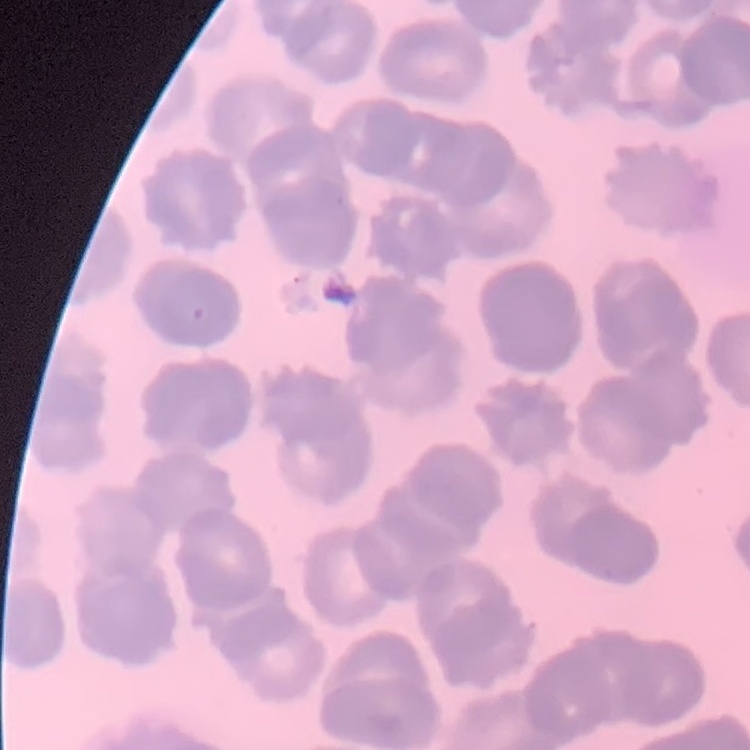
{
  "red_blood_cell_morphology": "rouleaux formation",
  "stain": "Field's or Giemsa",
  "preparation": "thin blood film",
  "image_type": "square crop of a larger photomicrograph"
}